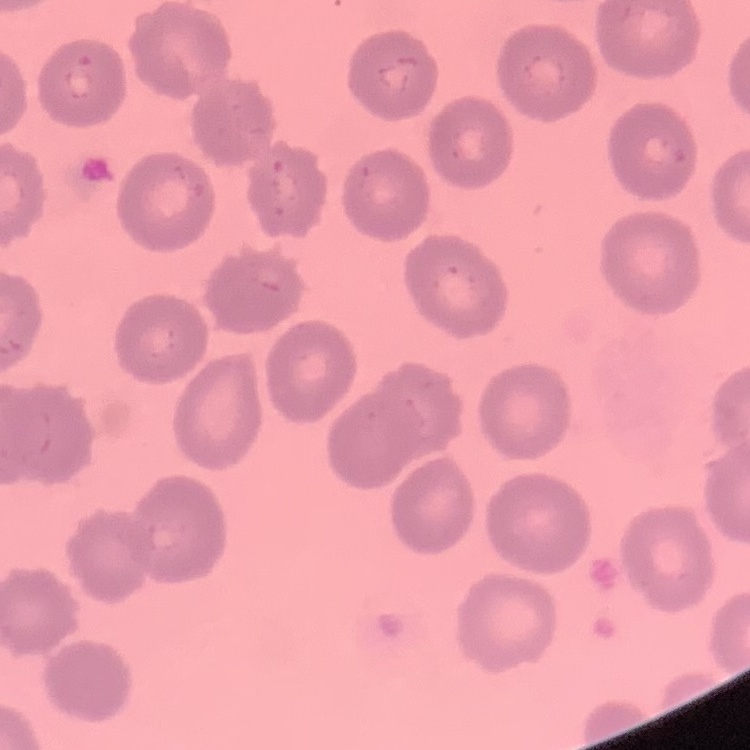
{
  "red_blood_cell_morphology": "no rouleaux formation",
  "stain": "Field's or Giemsa",
  "preparation": "thin blood smear",
  "image_type": "square crop of a larger photomicrograph"
}